Assess this cell for malaria.
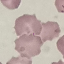
It is uninfected.

Summary:
  - Preparation: thin smear
  - Image type: automatically extracted cell patch, resized to 64 × 64 pixels
  - Stain: Giemsa
  - Capture: smartphone camera at the microscope eyepiece